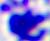

identification = leukocyte
magnification = 400x
modality = micrograph